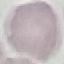
{
  "malaria_status": "uninfected",
  "image_type": "automatically extracted cell patch, resized to 64 × 64 pixels",
  "stain": "Giemsa",
  "capture": "smartphone through the microscope eyepiece",
  "preparation": "thin blood film"
}